Classify this cell by malaria status.
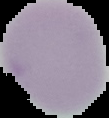

It is uninfected.

Image is 109×118 pixels. The area outside the segmented cell region is set to black. From a thin blood film.